Classify this cell by malaria status.
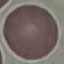
Uninfected.

image type = cell patch, automatically extracted from a larger field of view and resized to 64 × 64 pixels
preparation = thin smear
capture = smartphone through the microscope eyepiece
stain = Giemsa